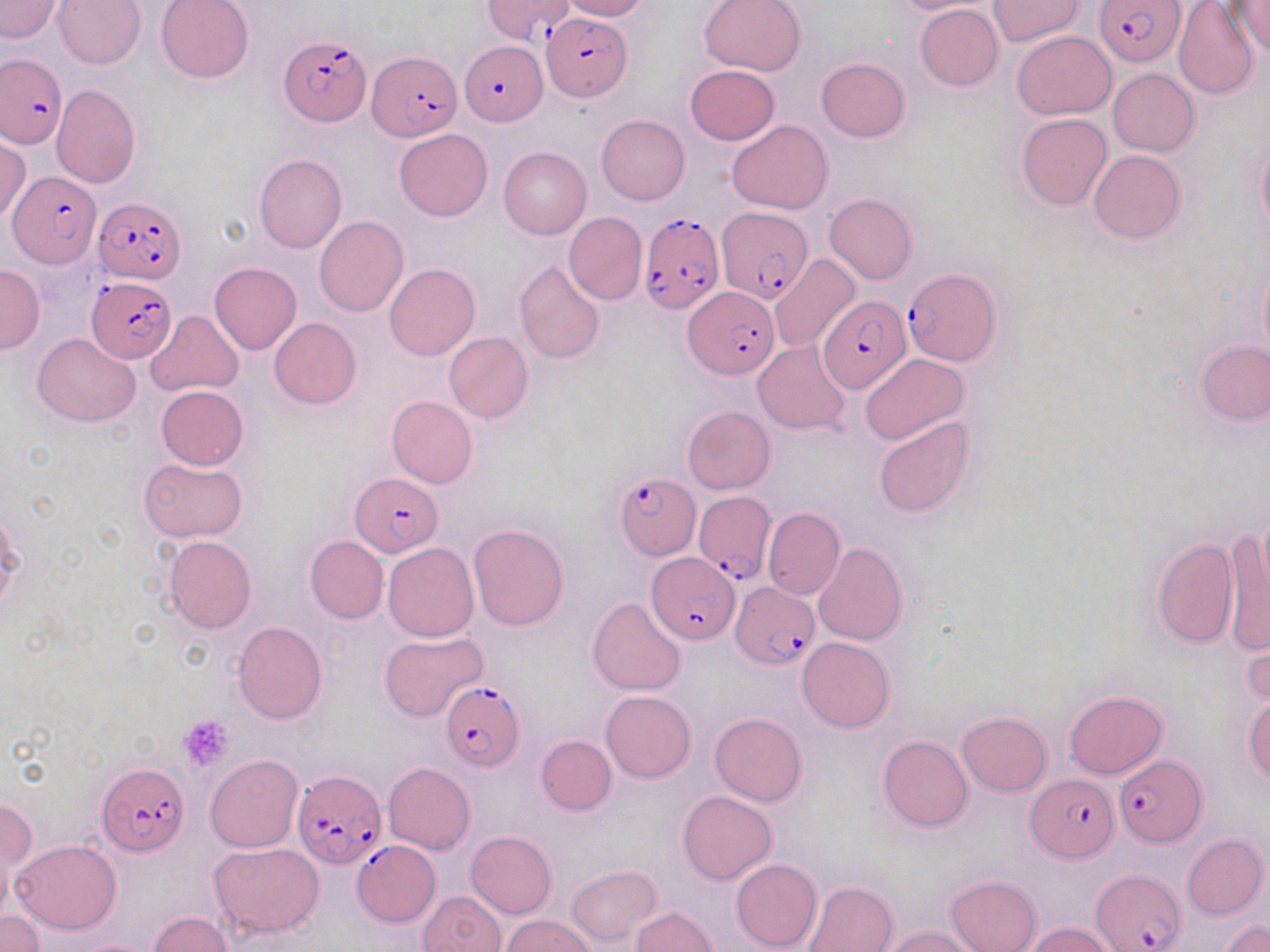

Approximate bounding boxes as [x1, y1, x2, y2] in pixels. Platelet locations: [178, 714, 234, 772]. Uninfected red blood cell locations: [53, 0, 145, 70], [155, 0, 255, 84], [561, 0, 649, 21], [698, 0, 806, 76], [887, 0, 993, 14], [1226, 0, 1270, 59], [0, 1, 63, 42], [987, 1, 1084, 47], [1173, 2, 1260, 102], [914, 4, 1003, 91], [1012, 31, 1118, 120], [815, 57, 909, 143], [685, 65, 780, 145], [1108, 68, 1200, 156], [52, 84, 142, 188], [1016, 113, 1112, 209], [597, 114, 690, 205], [727, 119, 833, 214], [393, 128, 492, 221], [0, 136, 31, 223], [1256, 136, 1270, 240], [499, 146, 591, 241], [1088, 150, 1186, 244], [254, 153, 348, 253], [824, 193, 918, 284], [564, 211, 647, 305], [314, 216, 409, 317], [771, 255, 860, 357], [514, 258, 606, 365], [1258, 260, 1270, 362], [210, 262, 301, 354], [0, 264, 46, 352], [384, 264, 480, 361], [146, 309, 244, 397], [269, 317, 362, 409], [444, 332, 534, 422], [32, 334, 141, 425], [753, 341, 851, 435], [1197, 341, 1270, 424], [860, 354, 970, 446], [156, 385, 249, 470], [386, 395, 478, 488], [682, 405, 776, 494], [874, 415, 975, 518], [138, 458, 248, 542], [763, 507, 845, 600], [468, 522, 569, 629], [1222, 529, 1270, 658], [164, 535, 256, 633], [304, 536, 389, 623], [1151, 536, 1239, 649], [383, 543, 480, 642], [814, 543, 908, 645], [588, 598, 686, 695], [233, 621, 328, 723], [1242, 626, 1269, 714], [379, 631, 490, 720], [797, 637, 894, 733], [601, 689, 696, 782], [1064, 689, 1168, 779], [1243, 694, 1270, 784], [709, 712, 807, 805], [957, 712, 1052, 796], [535, 735, 616, 814], [878, 735, 972, 831], [206, 755, 303, 853], [383, 762, 475, 854], [677, 790, 777, 884], [1, 793, 37, 901], [466, 830, 556, 918], [1181, 833, 1267, 919], [11, 839, 122, 934], [210, 842, 325, 938], [731, 858, 822, 951], [565, 864, 662, 947], [945, 875, 1041, 952], [804, 880, 898, 952], [418, 890, 506, 952], [630, 906, 717, 952], [0, 910, 44, 951], [147, 910, 235, 951], [501, 914, 597, 952], [1222, 920, 1270, 952], [1024, 923, 1116, 952], [883, 926, 978, 951]. Plasmodium falciparum-infected red blood cell locations: [1093, 0, 1187, 66], [541, 12, 631, 100], [278, 36, 369, 129], [460, 42, 547, 125], [366, 50, 461, 141], [1, 52, 66, 148], [10, 172, 99, 268], [94, 195, 186, 285], [717, 207, 814, 301], [636, 212, 724, 316], [902, 266, 1001, 364], [86, 278, 177, 363], [684, 287, 777, 379], [822, 296, 909, 393], [350, 473, 443, 556], [614, 474, 700, 559], [694, 488, 776, 584], [646, 552, 740, 643], [730, 581, 819, 670], [442, 681, 525, 770], [1114, 754, 1205, 847], [97, 763, 191, 856], [292, 767, 385, 868], [1027, 775, 1114, 861], [352, 841, 440, 927], [1093, 870, 1186, 950]. Slide-level diagnosis: Plasmodium falciparum. 1000x magnification. May-Grünwald-Giemsa stain. Single field of view. Thin blood film. Light microscopy. Image is 1270×952 pixels.